Identify the cell.
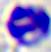

This is a leukocyte.

magnification = 400x
modality = micrograph